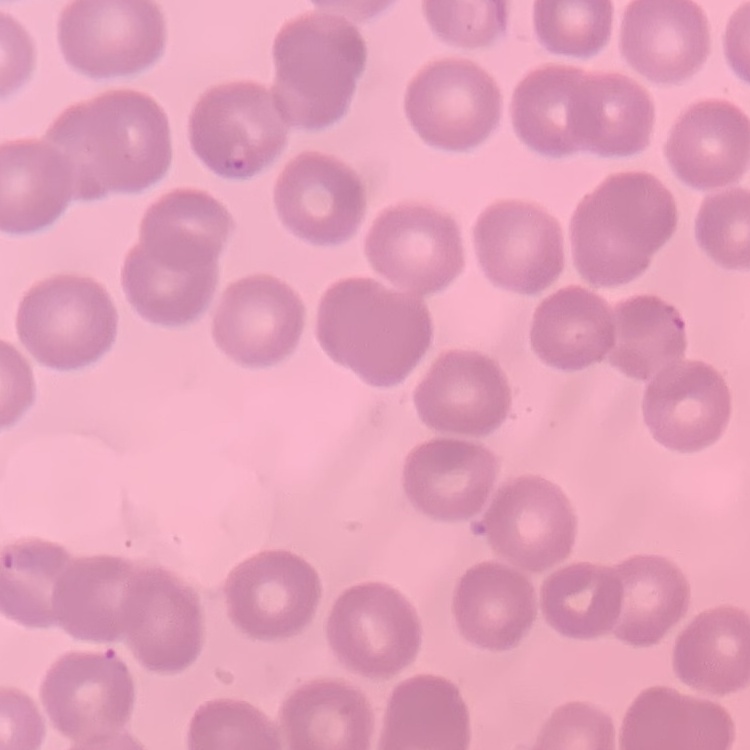 The red blood cells exhibit no rouleaux formation. Field's or Giemsa stain. Square crop of a larger photomicrograph. Thin blood film.